Name the cell type shown.
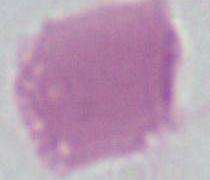
An erythrocyte.

Summary:
  - Magnification: 1000x
  - Modality: micrograph